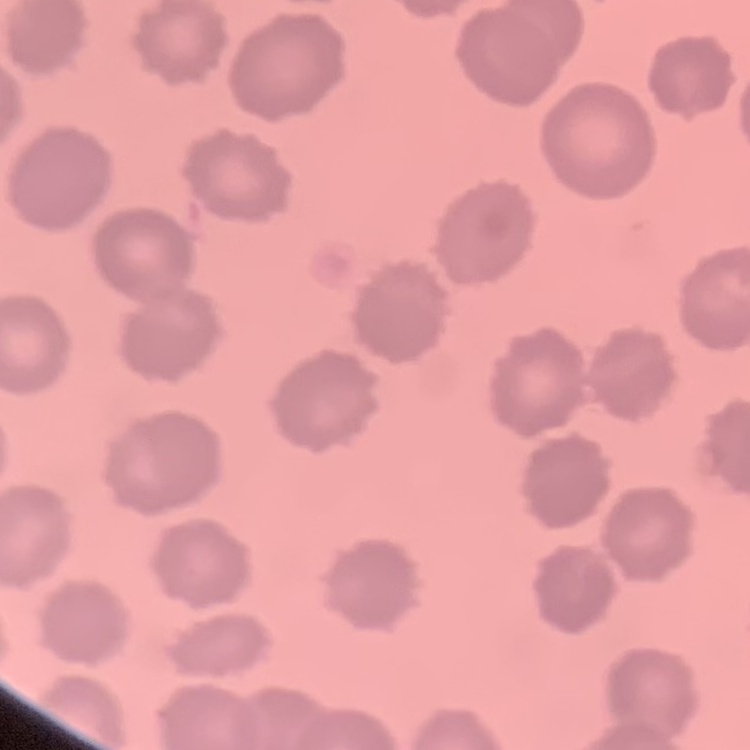

erythrocyte morphology = no rouleaux formation
image type = square crop of a larger photomicrograph
stain = Field's or Giemsa
preparation = thin peripheral smear